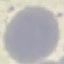
malaria status = uninfected
stain = Giemsa
capture = smartphone through the microscope eyepiece
preparation = thin smear
image type = cell patch, automatically extracted from a larger field of view and resized to 64 × 64 pixels